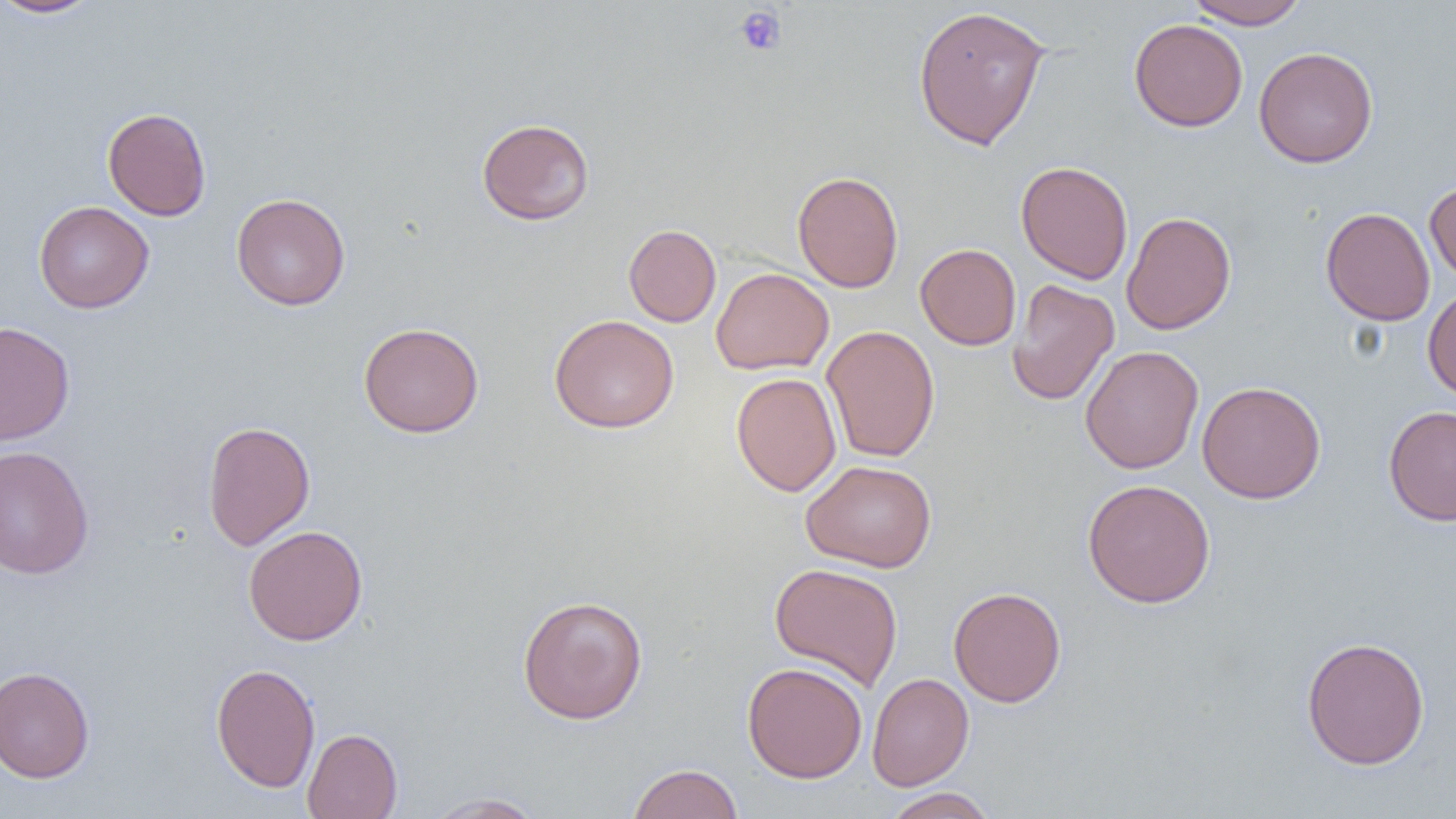

Approximate bounding boxes as (x1,y1)-(x2,y2) corner pairs in pixels. Uninfected red blood cell locations: (0,0)-(103,18), (1185,0)-(1309,29), (911,4)-(1052,151), (1129,18)-(1248,132), (1254,46)-(1378,168), (102,107)-(212,221), (476,118)-(595,225), (1016,160)-(1133,285), (791,171)-(904,292), (1425,179)-(1456,286), (230,192)-(350,311), (34,200)-(154,313), (1320,207)-(1436,326), (1121,211)-(1236,335), (624,224)-(722,327), (915,243)-(1021,350), (710,267)-(834,375), (1006,279)-(1120,406), (1422,286)-(1456,401), (549,314)-(679,433), (0,321)-(75,446), (358,322)-(484,438), (821,325)-(940,463), (1080,345)-(1204,474), (731,372)-(841,497), (1197,380)-(1326,504), (1383,405)-(1456,525), (202,420)-(315,551), (0,445)-(95,579), (801,459)-(937,572), (1082,478)-(1216,608), (243,525)-(368,645), (769,562)-(904,691), (948,586)-(1066,707), (517,594)-(648,725), (1301,636)-(1430,769), (210,662)-(320,793), (742,662)-(867,783), (0,665)-(95,783), (867,672)-(974,790), (302,728)-(403,819), (627,762)-(744,819), (883,788)-(997,819), (421,792)-(547,818). Platelet locations: (734,6)-(787,56). Slide-level diagnosis: no evidence of blood parasites. Captured at 1000x magnification. Thin blood film. Single field of view. Light microscopy. Image is 1456×819 pixels.